Classify this cell by malaria status.
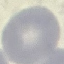

Uninfected.

stain: Giemsa
image_type: automatically extracted cell patch, resized to 64 × 64 pixels
capture: smartphone through the microscope eyepiece
preparation: thin smear